Report the malaria status of this cell.
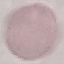

Uninfected.

Summary:
  - Stain: Giemsa
  - Image type: cell patch, automatically extracted from a larger field of view and resized to 64 × 64 pixels
  - Preparation: thin smear
  - Capture: smartphone through the microscope eyepiece